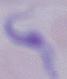

modality: micrograph
magnification: 1000x
identification: trypanosome